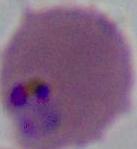
identification: Plasmodium
modality: micrograph
magnification: 400x or 1000x